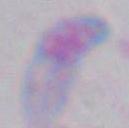

{
  "magnification": "1000x",
  "identification": "Toxoplasma gondii",
  "modality": "micrograph"
}